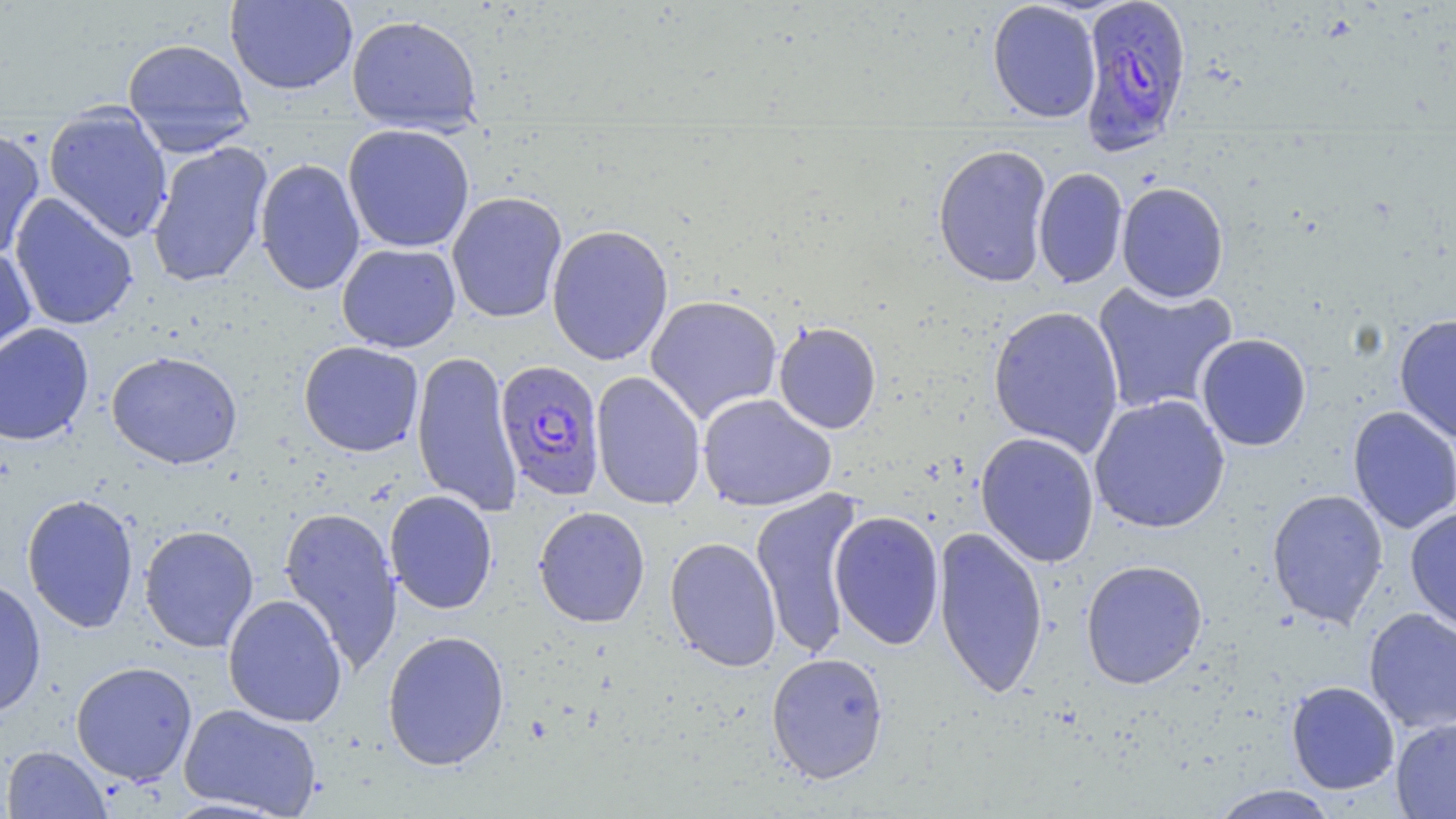 Approximate bounding boxes as named x1/y1/x2/y2 corners in pixels. Uninfected red blood cell locations: (x1=225, y1=0, x2=358, y2=95), (x1=986, y1=1, x2=1102, y2=123), (x1=346, y1=13, x2=483, y2=134), (x1=122, y1=37, x2=255, y2=150), (x1=43, y1=109, x2=173, y2=244), (x1=342, y1=123, x2=475, y2=253), (x1=0, y1=127, x2=46, y2=262), (x1=147, y1=141, x2=273, y2=288), (x1=932, y1=143, x2=1052, y2=288), (x1=254, y1=158, x2=366, y2=296), (x1=1033, y1=167, x2=1128, y2=289), (x1=1116, y1=181, x2=1229, y2=303), (x1=447, y1=191, x2=568, y2=323), (x1=10, y1=193, x2=139, y2=331), (x1=546, y1=224, x2=674, y2=366), (x1=0, y1=243, x2=36, y2=366), (x1=337, y1=243, x2=461, y2=352), (x1=1091, y1=281, x2=1238, y2=416), (x1=644, y1=295, x2=783, y2=424), (x1=987, y1=305, x2=1125, y2=457), (x1=1394, y1=313, x2=1456, y2=444), (x1=773, y1=320, x2=882, y2=434), (x1=0, y1=322, x2=94, y2=446), (x1=1196, y1=333, x2=1312, y2=451), (x1=298, y1=340, x2=424, y2=457), (x1=412, y1=349, x2=522, y2=517), (x1=106, y1=350, x2=243, y2=469), (x1=591, y1=371, x2=706, y2=510), (x1=698, y1=393, x2=837, y2=512), (x1=1089, y1=394, x2=1231, y2=534), (x1=1347, y1=406, x2=1456, y2=534), (x1=975, y1=431, x2=1100, y2=568), (x1=750, y1=488, x2=865, y2=659), (x1=1266, y1=488, x2=1389, y2=629), (x1=384, y1=489, x2=498, y2=614), (x1=22, y1=493, x2=139, y2=633), (x1=278, y1=505, x2=404, y2=675), (x1=533, y1=505, x2=650, y2=628), (x1=1405, y1=507, x2=1456, y2=634), (x1=829, y1=510, x2=945, y2=650), (x1=139, y1=524, x2=259, y2=653), (x1=933, y1=525, x2=1049, y2=700), (x1=664, y1=536, x2=782, y2=672), (x1=1080, y1=559, x2=1208, y2=689), (x1=0, y1=576, x2=47, y2=719), (x1=223, y1=593, x2=348, y2=727), (x1=1363, y1=607, x2=1456, y2=733), (x1=382, y1=629, x2=510, y2=771), (x1=766, y1=652, x2=889, y2=784), (x1=70, y1=661, x2=198, y2=785), (x1=1286, y1=681, x2=1400, y2=795), (x1=179, y1=703, x2=322, y2=817), (x1=1390, y1=717, x2=1456, y2=818), (x1=2, y1=745, x2=112, y2=819), (x1=1208, y1=784, x2=1340, y2=818). Plasmodium falciparum-infected red blood cell locations: (x1=1077, y1=0, x2=1193, y2=156), (x1=495, y1=360, x2=606, y2=501). Slide-level diagnosis: Plasmodium falciparum. One field of a larger specimen. Light microscopy. Thin blood film. Captured at 1000x magnification. May-Grünwald-Giemsa stain. Image is 1456×819 pixels.